Report the malaria status of this cell.
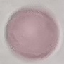

It is uninfected.

image type = cell patch, automatically extracted from a larger field of view and resized to 64 × 64 pixels
preparation = thin blood film
stain = Giemsa
capture = smartphone camera at the microscope eyepiece